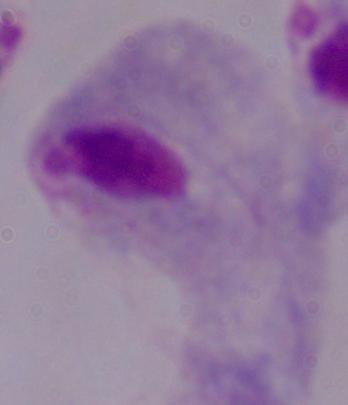

{
  "magnification": "1000x",
  "modality": "photomicrograph",
  "identification": "trichomonad"
}